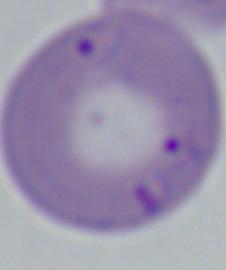 1000x magnification. Micrograph. A Babesia parasite is seen.